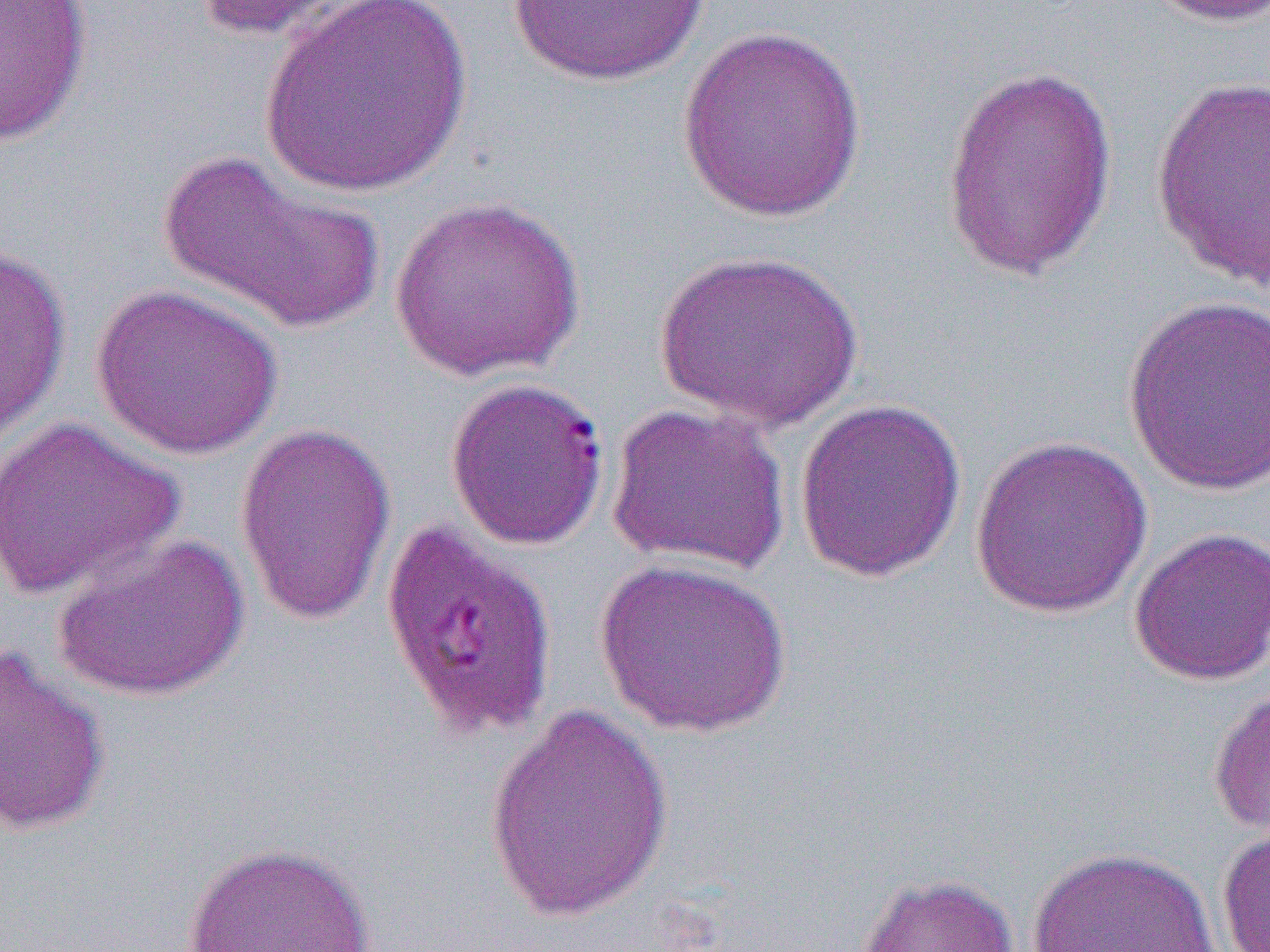 Approximate bounding boxes as (x1, y1, x2, y2) in pixels. Plasmodium falciparum-infected red blood cell locations: (445, 376, 612, 551), (380, 518, 560, 741). Uninfected red blood cell locations: (0, 0, 94, 144), (189, 0, 363, 42), (508, 0, 709, 86), (1141, 0, 1270, 28), (257, 1, 474, 197), (675, 24, 869, 223), (940, 63, 1118, 283), (1150, 74, 1269, 291), (156, 148, 385, 339), (389, 196, 586, 381), (0, 237, 72, 454), (653, 248, 864, 431), (89, 283, 284, 460), (1122, 294, 1270, 497), (793, 397, 968, 583), (605, 402, 791, 576), (1, 416, 184, 600), (234, 423, 397, 626), (968, 434, 1154, 619), (1128, 527, 1270, 686), (51, 531, 250, 703), (593, 557, 792, 738), (0, 642, 112, 839), (1207, 679, 1270, 844), (483, 700, 676, 922), (1216, 821, 1270, 952), (180, 842, 379, 951), (1026, 846, 1220, 952), (854, 872, 1020, 952). Slide-level diagnosis: Plasmodium falciparum. 1000x magnification. Image is 1270×952 pixels. Optical microscopy. One field of a larger specimen. Thin blood film.